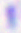
{
  "modality": "photomicrograph",
  "identification": "Toxoplasma gondii",
  "magnification": "400x"
}